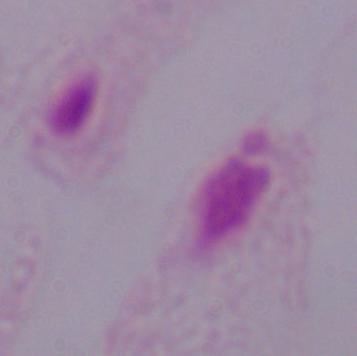
identification = trichomonad
magnification = 1000x
modality = micrograph